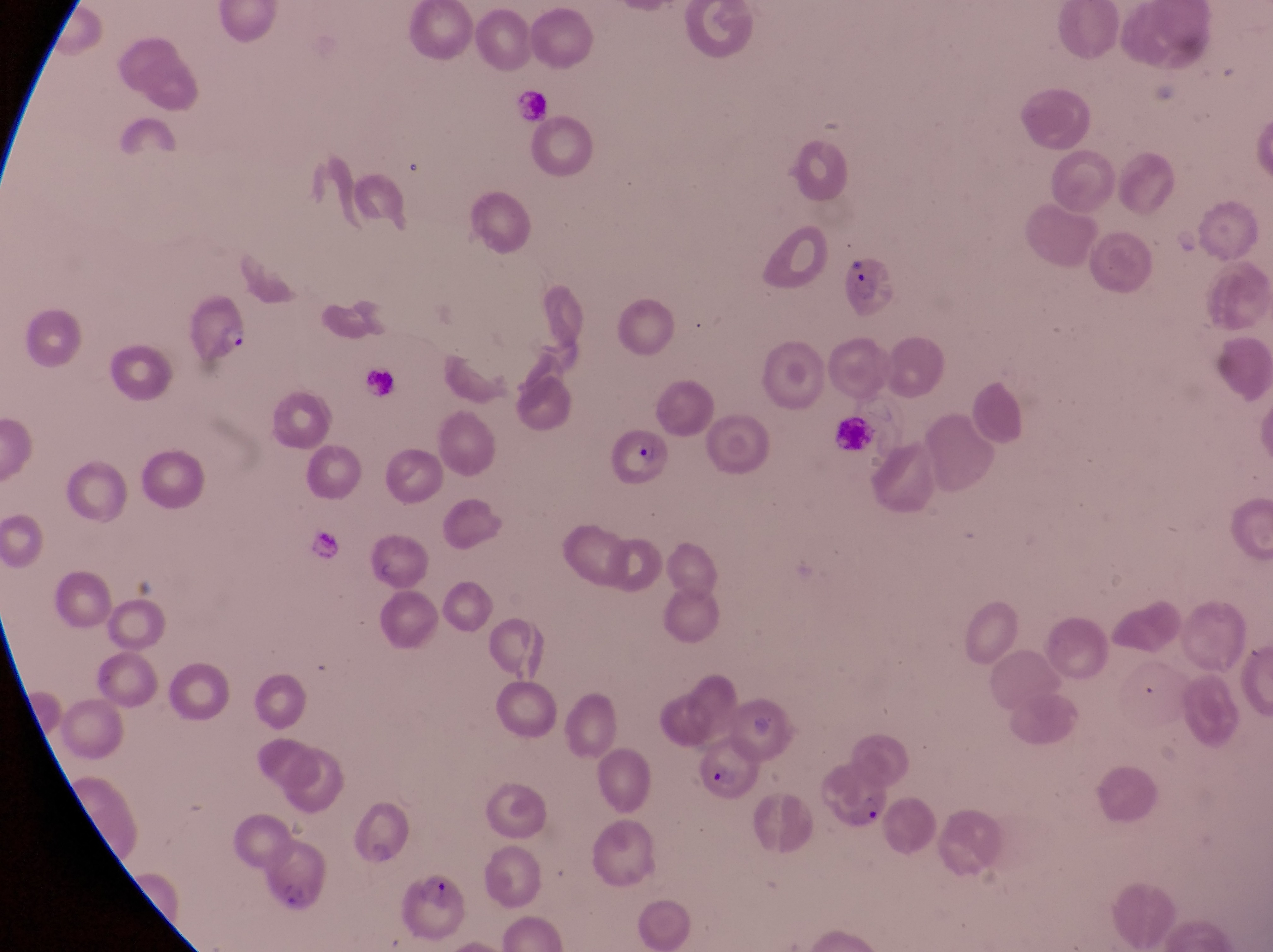

parasitised red blood cell locations = approximate bounding boxes as {left, top, right, bottom} in pixels: {836, 255, 899, 320}, {180, 287, 254, 361}, {604, 429, 674, 486}, {691, 734, 765, 802}, {809, 762, 889, 844}, {260, 839, 325, 911}, {387, 876, 474, 946}
magnification = 1000x
preparation = thin blood film
field of view = single
artifact (platelet-like body, stain precipitate, or debris) locations = approximate bounding boxes as {left, top, right, bottom} in pixels: {512, 88, 553, 124}
country = Uganda
capture = smartphone photograph through the eyepiece of an Olympus CX-23 microscope
image size = 1273×952 pixels
leukocyte locations = approximate bounding boxes as {left, top, right, bottom} in pixels: {360, 364, 399, 403}, {834, 417, 880, 456}, {307, 528, 357, 566}